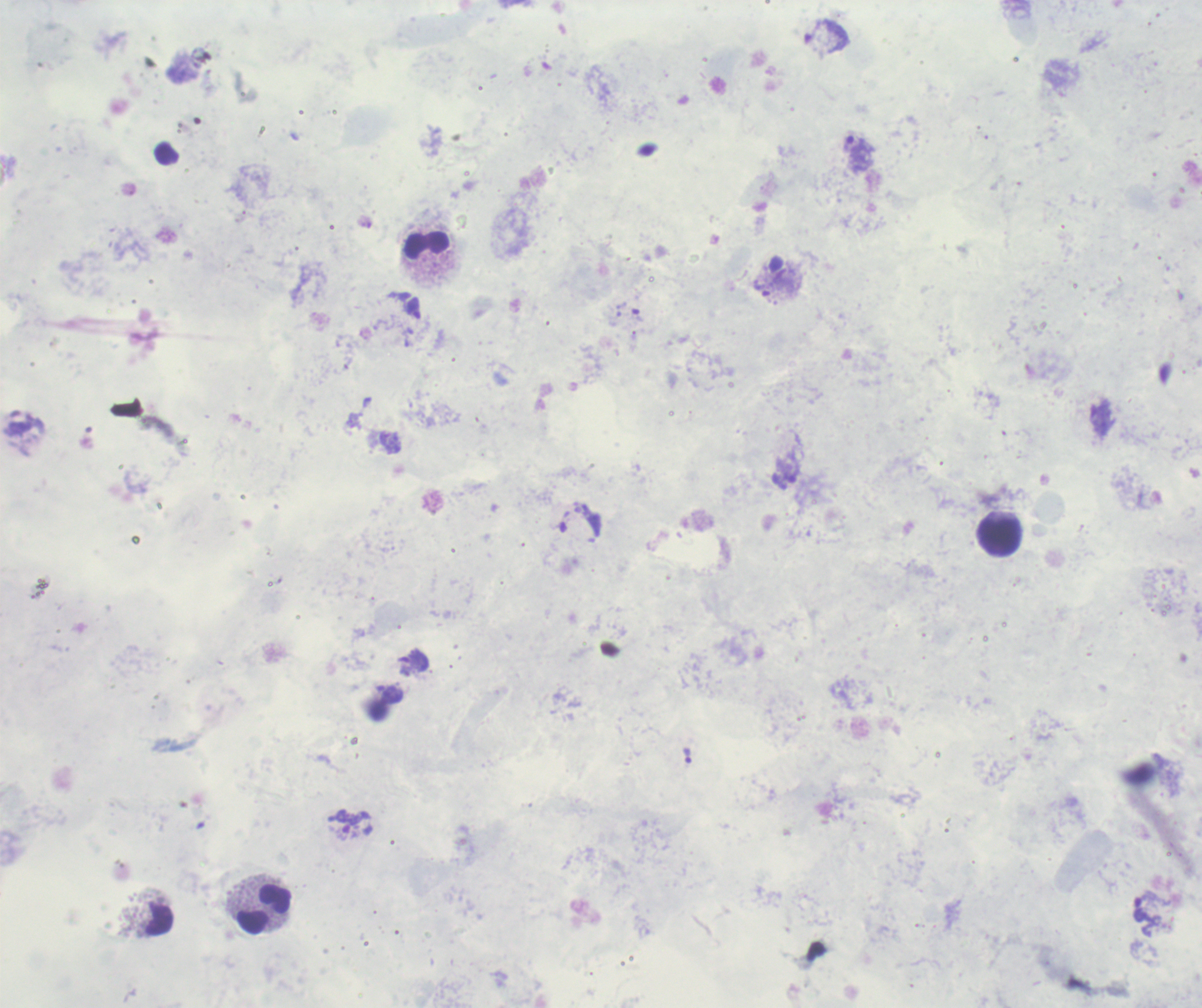 Approximate centers as {x, y} in pixels. Leukocyte locations: {426, 246}, {999, 536}, {265, 909}. Trophozoite locations: {858, 152}, {767, 290}, {413, 309}, {415, 661}, {687, 755}. Romanowsky stain. 100x magnification. One field from this slide. Result: positive for Plasmodium parasites. Image is 1202×1008 pixels. Previously used in an actual diagnosis. Thick smear of blood. Background quality: poor.